State the preparation type.
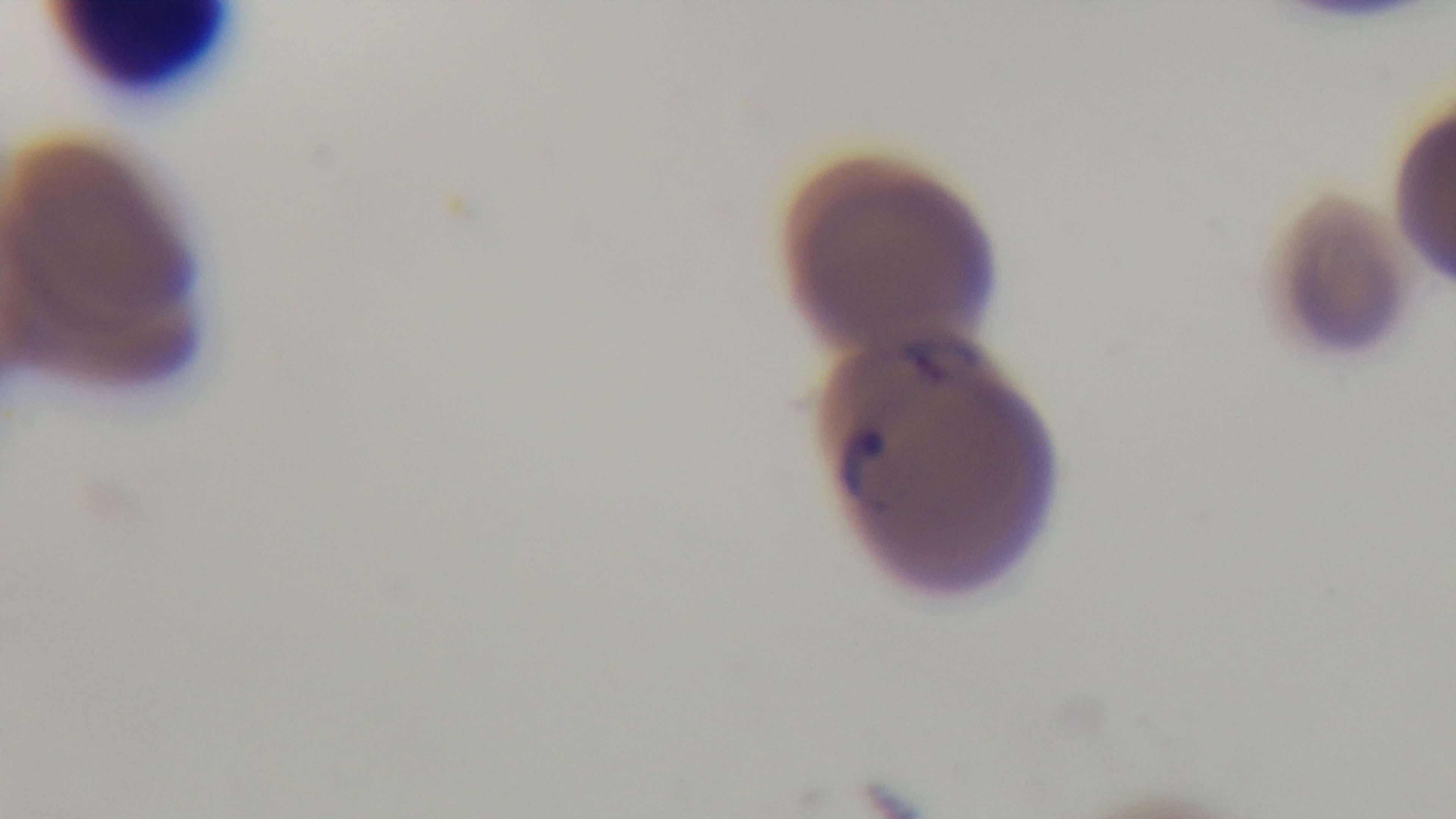

A thin smear.

Mounted 4K digital camera. Malaria status: infected. 100x oil-immersion objective. Giemsa-stained. Light microscopy. One field from the slide.